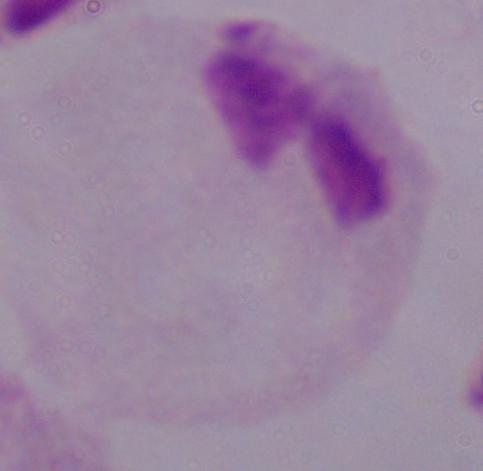
Micrograph. 1000x magnification. A trichomonad is shown.